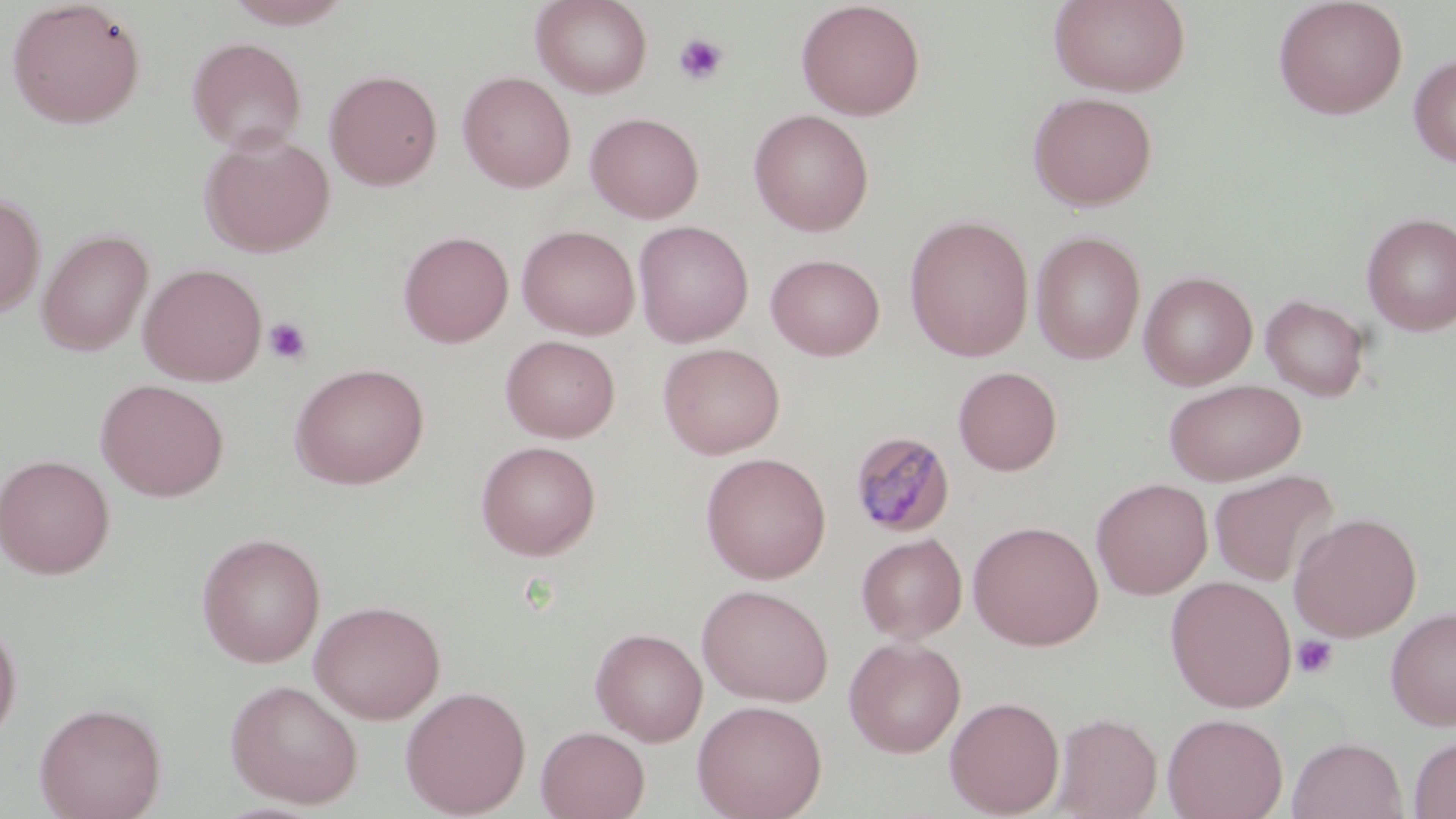

Summary:
  - Coordinate format: approximate bounding boxes as (x1,y1)-(x2,y2) corner pairs in pixels
  - Platelet locations: (673,32)-(729,85), (264,317)-(312,366), (1292,635)-(1338,679)
  - Uninfected red blood cell locations: (5,0)-(147,129), (223,0)-(356,29), (531,0)-(653,98), (1049,0)-(1190,97), (1273,0)-(1408,120), (795,1)-(926,120), (187,37)-(307,154), (1408,53)-(1456,167), (324,68)-(443,190), (457,70)-(576,193), (1028,90)-(1158,211), (749,109)-(875,236), (585,111)-(704,223), (199,131)-(336,258), (0,192)-(46,318), (1361,212)-(1456,336), (904,213)-(1035,361), (633,220)-(754,347), (516,224)-(640,340), (37,228)-(154,356), (398,230)-(514,348), (1030,230)-(1146,364), (765,253)-(885,361), (138,263)-(268,387), (1138,271)-(1257,390), (1261,294)-(1370,401), (500,335)-(620,443), (658,342)-(785,459), (290,362)-(429,489), (953,366)-(1062,476), (95,379)-(229,501), (1163,379)-(1306,486), (475,440)-(601,560), (700,452)-(832,584), (1,454)-(116,579), (1208,469)-(1338,587), (1091,478)-(1213,600), (1289,512)-(1422,641), (968,519)-(1104,651), (195,532)-(326,667), (856,532)-(967,644), (1166,575)-(1297,712), (697,583)-(834,706), (309,599)-(446,723), (1386,606)-(1456,730), (0,615)-(23,749), (590,626)-(708,746), (844,636)-(966,758), (225,678)-(364,808), (400,685)-(531,818), (944,695)-(1065,817), (691,699)-(828,819), (34,701)-(167,819), (1051,712)-(1162,818), (1162,712)-(1288,819), (536,725)-(650,819), (1408,734)-(1456,819), (1287,736)-(1408,819)
  - Plasmodium malariae-infected red blood cell locations: (848,429)-(956,537)
  - Slide-level diagnosis: Plasmodium malariae
  - Modality: light microscopy
  - Field of view: one of a larger specimen
  - Magnification: 1000x
  - Stain: May-Grünwald-Giemsa
  - Preparation: thin blood film
  - Image size: 1456×819 pixels